Locate and identify every blood parasite.
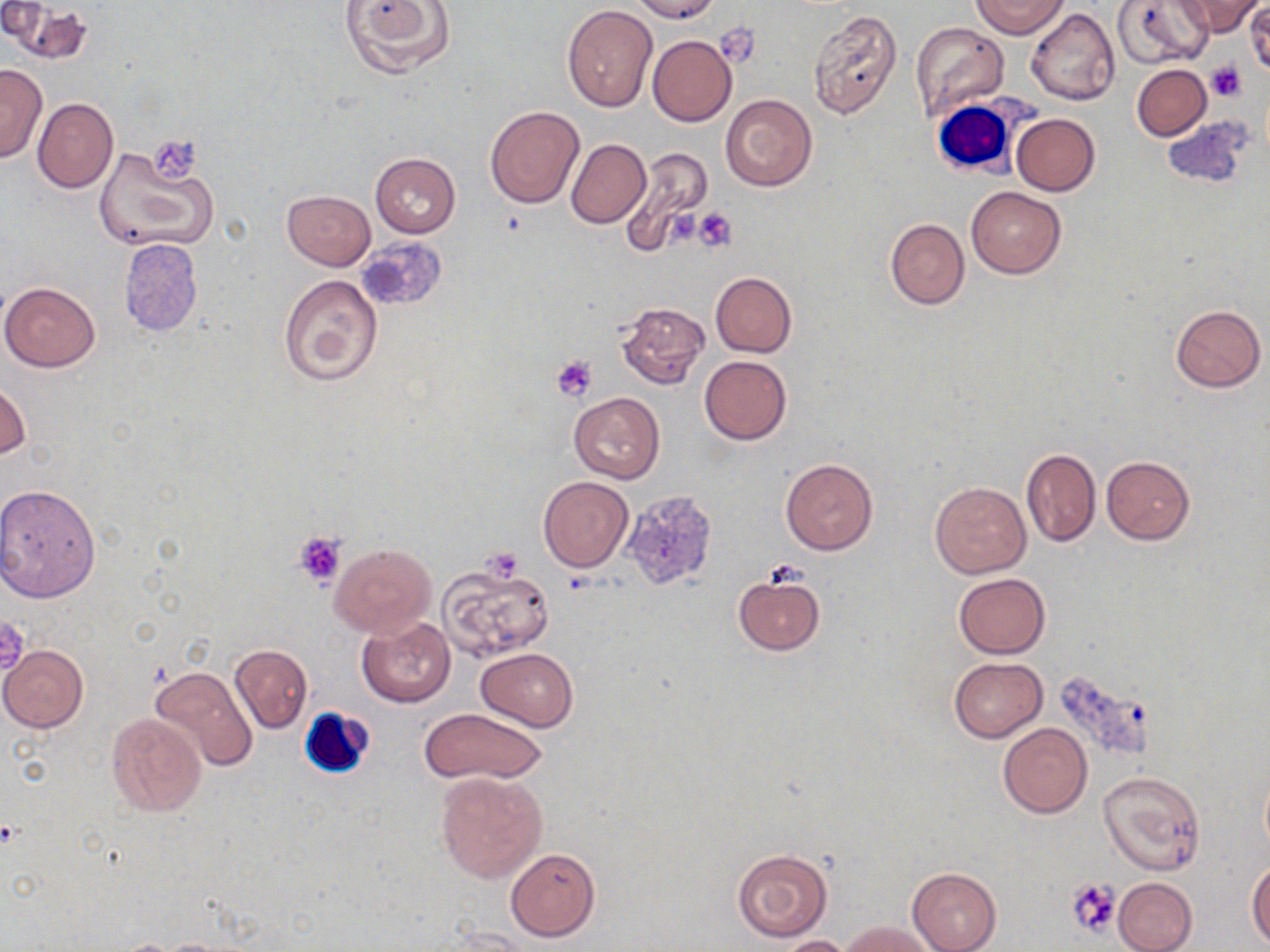

No blood parasites observed.

Summary:
  - Coordinate format: approximate bounding boxes as (x1,y1)-(x2,y2) corner pairs in pixels
  - Uninfected red blood cell locations: (342,0)-(454,78), (629,0)-(721,22), (973,0)-(1069,38), (1176,0)-(1262,38), (1,1)-(53,44), (1112,1)-(1213,70), (1245,1)-(1270,79), (9,3)-(90,61), (562,5)-(657,111), (804,7)-(902,121), (1026,7)-(1120,105), (911,22)-(1010,124), (647,35)-(737,127), (0,65)-(49,162), (1132,65)-(1212,140), (720,94)-(817,191), (33,98)-(118,193), (484,105)-(584,208), (1011,113)-(1100,195), (565,138)-(650,229), (94,143)-(218,252), (618,148)-(714,254), (370,152)-(461,238), (966,186)-(1066,278), (283,190)-(375,269), (885,218)-(969,309), (119,239)-(203,336), (710,272)-(796,357), (277,273)-(382,387), (1,281)-(101,372), (616,302)-(710,391), (1169,304)-(1265,391), (699,355)-(791,445), (1,382)-(31,461), (569,392)-(663,484), (1020,447)-(1100,547), (1101,455)-(1195,545), (780,459)-(877,555), (538,476)-(633,572), (930,481)-(1031,579), (0,483)-(102,600), (332,543)-(436,637), (438,560)-(555,661), (733,572)-(824,657), (954,572)-(1050,658), (357,618)-(455,707), (229,644)-(313,733), (1,645)-(87,732), (476,648)-(579,730), (950,657)-(1047,741), (148,665)-(258,773), (417,707)-(547,784), (106,713)-(205,817), (997,722)-(1092,819), (1259,762)-(1270,859), (1097,771)-(1206,876), (436,772)-(547,883), (505,847)-(600,941), (732,849)-(834,943), (1247,860)-(1270,946), (908,867)-(1002,952), (1113,877)-(1197,952), (840,920)-(937,952), (448,926)-(536,951), (774,935)-(854,952)
  - White blood cell locations: (929,96)-(1023,178), (300,706)-(374,777)
  - Platelet locations: (716,24)-(761,66), (1206,61)-(1246,103), (694,208)-(737,253), (551,355)-(597,402), (293,532)-(345,586), (0,616)-(30,678), (1067,878)-(1121,940)
  - Slide-level diagnosis: no evidence of blood parasites
  - Magnification: 1000x
  - Preparation: thin blood film
  - Field of view: one of a larger specimen
  - Image size: 1270×952 pixels
  - Stain: May-Grünwald-Giemsa
  - Modality: light microscopy